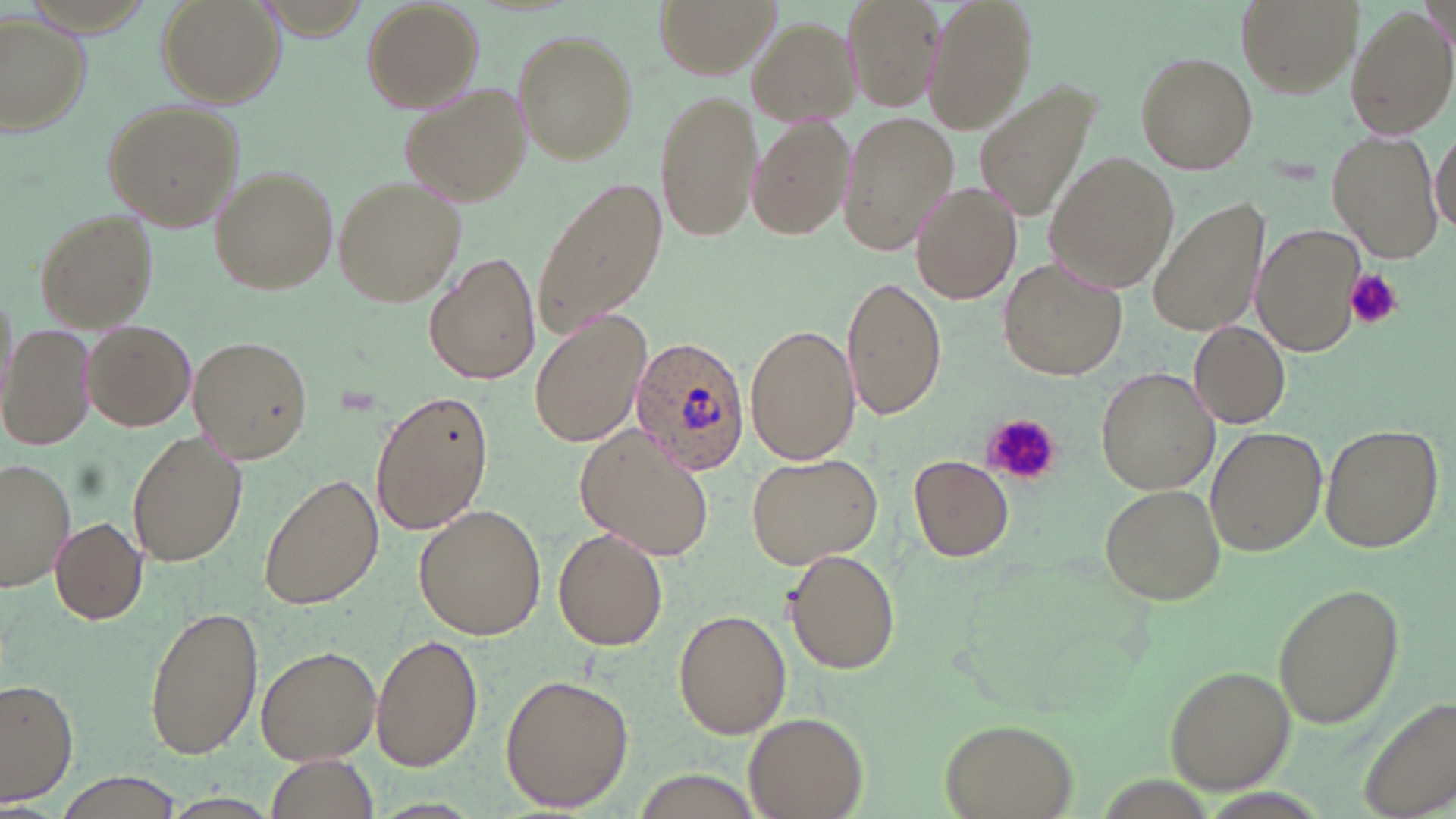

Approximate bounding boxes as named x1/y1/x2/y2 corners in pixels. Plasmodium ovale-infected red blood cell locations: (x1=628, y1=333, x2=751, y2=474). Platelet locations: (x1=1346, y1=268, x2=1401, y2=329), (x1=980, y1=414, x2=1058, y2=483). Uninfected red blood cell locations: (x1=157, y1=0, x2=285, y2=108), (x1=360, y1=0, x2=483, y2=111), (x1=654, y1=0, x2=777, y2=78), (x1=844, y1=0, x2=945, y2=112), (x1=921, y1=0, x2=1037, y2=136), (x1=1236, y1=0, x2=1358, y2=97), (x1=1346, y1=5, x2=1455, y2=139), (x1=1, y1=12, x2=92, y2=135), (x1=751, y1=17, x2=863, y2=127), (x1=512, y1=29, x2=637, y2=164), (x1=1135, y1=51, x2=1259, y2=174), (x1=398, y1=82, x2=527, y2=205), (x1=656, y1=90, x2=761, y2=245), (x1=979, y1=93, x2=1092, y2=224), (x1=102, y1=99, x2=243, y2=230), (x1=840, y1=110, x2=959, y2=254), (x1=747, y1=115, x2=857, y2=242), (x1=1326, y1=129, x2=1444, y2=261), (x1=1429, y1=130, x2=1456, y2=235), (x1=1046, y1=152, x2=1178, y2=293), (x1=208, y1=166, x2=337, y2=294), (x1=532, y1=174, x2=666, y2=341), (x1=332, y1=175, x2=467, y2=307), (x1=911, y1=180, x2=1022, y2=305), (x1=1149, y1=199, x2=1266, y2=336), (x1=34, y1=208, x2=159, y2=331), (x1=1253, y1=222, x2=1368, y2=359), (x1=424, y1=250, x2=541, y2=385), (x1=998, y1=256, x2=1132, y2=382), (x1=842, y1=273, x2=945, y2=422), (x1=529, y1=311, x2=652, y2=448), (x1=3, y1=321, x2=99, y2=451), (x1=82, y1=321, x2=196, y2=430), (x1=746, y1=321, x2=859, y2=468), (x1=1190, y1=322, x2=1292, y2=426), (x1=188, y1=334, x2=313, y2=464), (x1=1096, y1=366, x2=1216, y2=496), (x1=371, y1=387, x2=494, y2=537), (x1=1319, y1=422, x2=1444, y2=552), (x1=128, y1=427, x2=250, y2=567), (x1=1205, y1=427, x2=1326, y2=554), (x1=576, y1=429, x2=714, y2=561), (x1=746, y1=450, x2=883, y2=568), (x1=908, y1=455, x2=1013, y2=560), (x1=0, y1=458, x2=77, y2=592), (x1=258, y1=470, x2=384, y2=613), (x1=1101, y1=484, x2=1223, y2=604), (x1=414, y1=502, x2=548, y2=638), (x1=49, y1=515, x2=148, y2=625), (x1=553, y1=526, x2=669, y2=649), (x1=783, y1=549, x2=900, y2=675), (x1=1273, y1=583, x2=1403, y2=730), (x1=144, y1=604, x2=263, y2=760), (x1=673, y1=609, x2=792, y2=738), (x1=371, y1=632, x2=483, y2=770), (x1=256, y1=644, x2=383, y2=765), (x1=1167, y1=666, x2=1293, y2=791), (x1=500, y1=672, x2=635, y2=811), (x1=1, y1=679, x2=78, y2=807), (x1=1359, y1=699, x2=1456, y2=818), (x1=743, y1=713, x2=868, y2=818), (x1=940, y1=717, x2=1078, y2=819), (x1=262, y1=756, x2=381, y2=817), (x1=52, y1=774, x2=191, y2=819). Slide-level diagnosis: Plasmodium ovale. Light microscopy. 1000x magnification. Single field of view. Thin blood smear. Image is 1456×819 pixels. May-Grünwald-Giemsa-stained preparation.